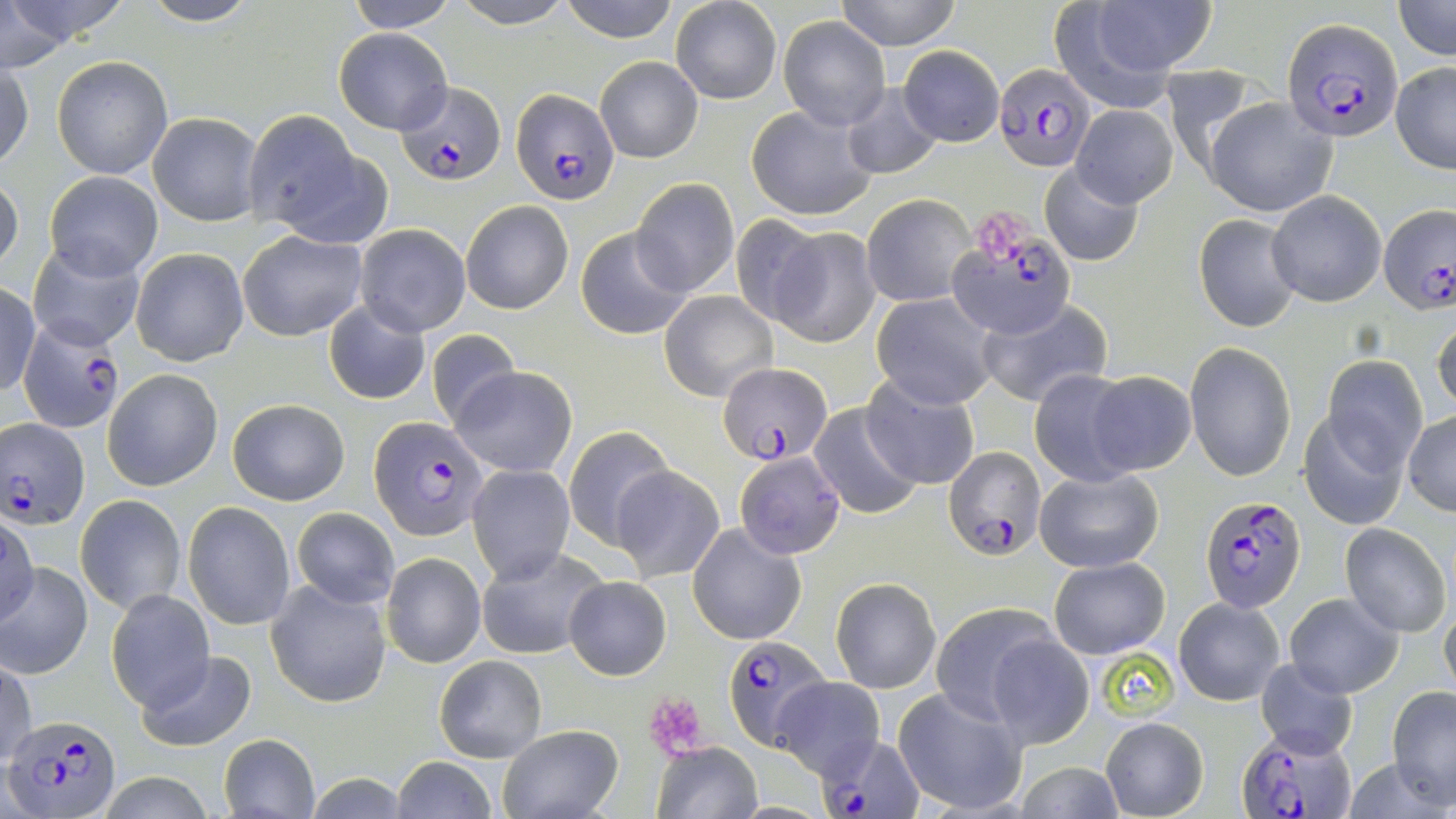

{
  "slide_level_diagnosis": "Plasmodium falciparum",
  "magnification": "1000x",
  "stain": "May-Grünwald-Giemsa",
  "plasmodium_falciparum_infected_red_blood_cell_locations": "approximate bounding boxes as [x1, y1, x2, y2] in pixels: [1282, 18, 1403, 142], [994, 63, 1096, 173], [395, 81, 507, 187], [512, 87, 617, 204], [1377, 206, 1454, 311], [949, 225, 1075, 338], [18, 321, 128, 432], [718, 363, 833, 463], [3, 417, 91, 530], [368, 417, 486, 538], [945, 446, 1045, 560], [1198, 492, 1306, 610], [724, 636, 832, 752], [9, 715, 117, 814], [1240, 728, 1353, 817], [816, 733, 922, 819]",
  "image_size": "1456×819 pixels",
  "modality": "optical microscopy",
  "platelet_locations": "approximate bounding boxes as [x1, y1, x2, y2] in pixels: [975, 210, 1027, 261], [650, 695, 704, 759]",
  "field_of_view": "single",
  "uninfected_red_blood_cell_locations": "approximate bounding boxes as [x1, y1, x2, y2] in pixels: [139, 0, 263, 26], [449, 0, 579, 28], [559, 0, 680, 42], [835, 0, 961, 49], [1065, 0, 1214, 95], [0, 1, 92, 68], [343, 1, 458, 33], [1393, 1, 1455, 60], [670, 2, 782, 104], [777, 16, 891, 130], [334, 29, 452, 133], [899, 44, 1004, 147], [51, 55, 173, 179], [593, 55, 703, 163], [1, 57, 33, 171], [1390, 62, 1456, 174], [1160, 65, 1259, 176], [840, 82, 943, 180], [1204, 96, 1335, 218], [745, 104, 877, 221], [1072, 105, 1177, 206], [148, 111, 262, 227], [243, 111, 373, 237], [1038, 162, 1144, 267], [44, 170, 163, 280], [0, 172, 23, 278], [631, 178, 740, 297], [1267, 191, 1386, 307], [862, 194, 974, 307], [461, 200, 573, 314], [1193, 211, 1301, 332], [726, 216, 828, 327], [354, 224, 470, 336], [576, 226, 694, 341], [767, 227, 881, 349], [237, 231, 368, 341], [27, 243, 146, 351], [130, 247, 249, 367], [0, 284, 41, 397], [660, 290, 777, 401], [872, 292, 999, 409], [323, 300, 432, 406], [979, 301, 1110, 406], [1432, 314, 1456, 419], [424, 327, 524, 433], [1185, 343, 1296, 482], [1323, 357, 1427, 472], [449, 365, 578, 477], [103, 369, 223, 491], [1028, 369, 1140, 486], [1086, 370, 1196, 476], [862, 377, 981, 490], [227, 396, 351, 506], [809, 402, 923, 520], [1301, 405, 1409, 530], [1404, 411, 1455, 516], [563, 424, 674, 550], [734, 451, 846, 559], [467, 463, 574, 585], [611, 465, 725, 581], [1034, 468, 1163, 573], [76, 495, 186, 613], [182, 501, 297, 630], [292, 507, 399, 608], [0, 514, 39, 626], [690, 522, 806, 644], [1339, 523, 1452, 636], [476, 545, 608, 660], [381, 553, 486, 668], [1048, 557, 1170, 659], [1, 560, 93, 680], [564, 576, 671, 680], [831, 576, 941, 694], [265, 579, 393, 708], [106, 589, 214, 710], [1284, 593, 1403, 697], [1173, 597, 1284, 705], [929, 602, 1063, 725], [1438, 607, 1456, 702], [985, 632, 1095, 751], [134, 649, 257, 750], [434, 654, 549, 763], [1256, 656, 1359, 760], [1, 659, 36, 769], [773, 677, 884, 779], [1387, 686, 1456, 807], [892, 687, 1028, 816], [1101, 716, 1208, 819], [496, 725, 625, 819], [219, 733, 321, 818], [651, 742, 762, 819], [389, 755, 498, 819], [1014, 761, 1126, 819], [96, 774, 218, 817], [301, 774, 414, 817]",
  "preparation": "thin blood film"
}